Name the blood parasite species.
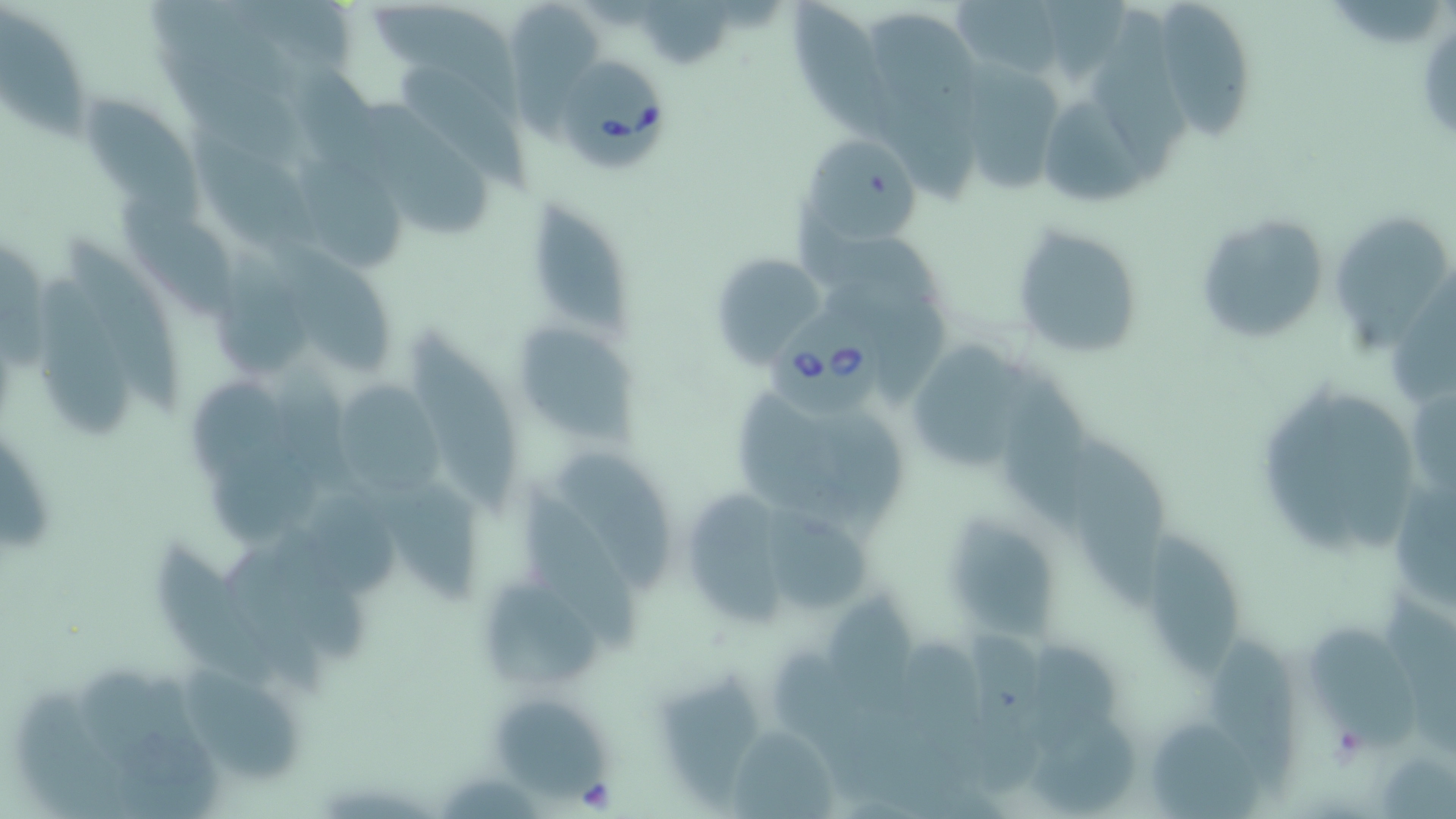

Babesia divergens.

field_of_view: single
uninfected_red_blood_cell_locations: 'approximate bounding boxes as (x1,y1)-(x2,y2) corner pairs in pixels: (513,0)-(596,134), (640,0)-(739,73), (788,0)-(905,150), (952,0)-(1064,75), (1042,0)-(1129,83), (1330,0)-(1444,49), (370,1)-(525,117), (1153,3)-(1260,134), (1087,8)-(1192,182), (0,9)-(86,143), (866,13)-(987,132), (157,41)-(300,164), (963,55)-(1062,194), (401,66)-(527,188), (83,93)-(204,223), (870,95)-(985,205), (356,96)-(490,237), (1043,100)-(1150,204), (188,128)-(325,259), (805,137)-(921,242), (294,154)-(406,270), (529,190)-(645,342), (114,195)-(239,320), (794,212)-(945,318), (1195,212)-(1331,346), (1334,216)-(1448,353), (1010,221)-(1145,359), (67,236)-(186,414), (273,240)-(392,375), (0,243)-(53,371), (212,249)-(313,374), (710,251)-(831,365), (1390,264)-(1456,403), (37,279)-(138,442), (827,279)-(951,402), (512,321)-(638,443), (408,329)-(520,509), (905,340)-(1032,473), (995,367)-(1095,536), (190,375)-(306,490), (1268,378)-(1362,553), (335,383)-(445,500), (735,387)-(841,526), (1410,395)-(1456,498), (1327,396)-(1418,552), (811,401)-(906,540), (1071,435)-(1167,613), (204,436)-(326,547), (557,449)-(677,595), (374,481)-(482,601), (519,482)-(643,651), (1390,486)-(1456,607), (687,490)-(789,626), (306,492)-(397,591), (761,508)-(875,615), (952,518)-(1055,646), (1144,530)-(1240,682), (157,541)-(281,689), (223,553)-(333,705), (489,579)-(606,686), (827,592)-(920,720), (1381,596)-(1456,694), (1304,624)-(1418,749), (960,630)-(1043,804), (1027,637)-(1118,763), (1209,639)-(1303,798), (903,640)-(989,793), (182,665)-(301,783), (75,666)-(225,812), (660,671)-(761,810), (15,688)-(145,819), (498,700)-(603,800), (1028,726)-(1139,815), (728,727)-(840,818), (445,775)-(541,819)'
magnification: 1000x
image_size: 1456×819 pixels
preparation: thin blood film
stain: May-Grünwald-Giemsa
modality: optical microscopy
babesia_divergens_infected_red_blood_cell_locations: 'approximate bounding boxes as (x1,y1)-(x2,y2) corner pairs in pixels: (560,59)-(670,174), (764,305)-(888,421)'